Describe the morphology of the red blood cells.
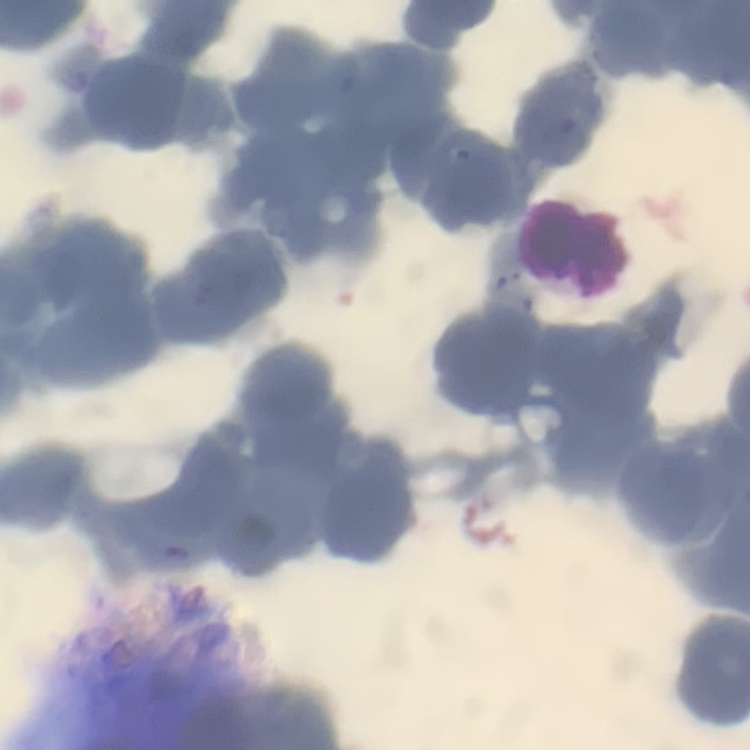
They show rouleaux formation.

Summary:
  - Image type: square crop of a larger photomicrograph
  - Stain: Field's or Giemsa
  - Preparation: thin blood smear